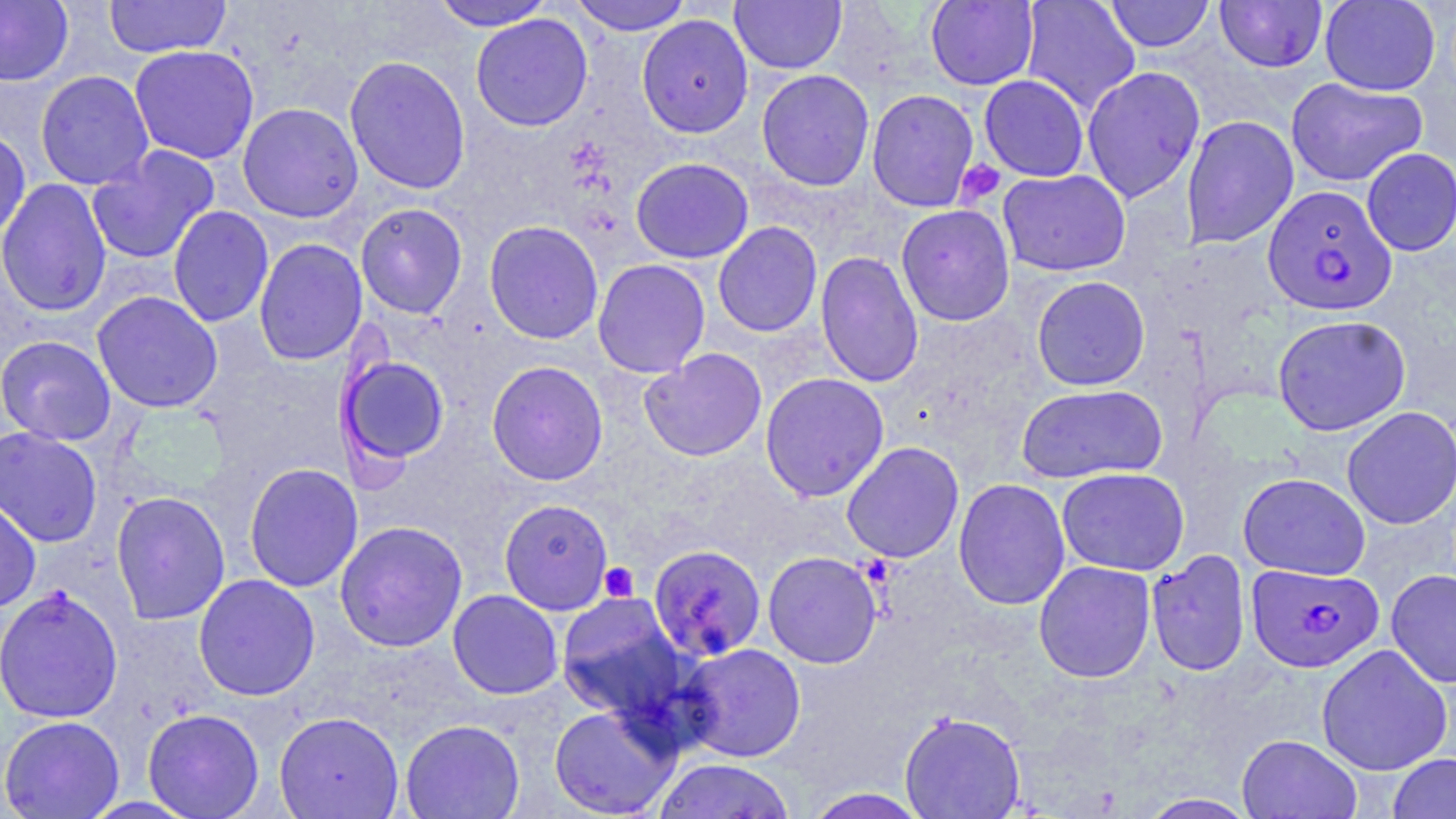

{
  "slide_level_diagnosis": "Plasmodium falciparum",
  "platelet_locations": "approximate bounding boxes as (x1,y1)-(x2,y2) corner pairs in pixels: (956,160)-(1006,205), (599,562)-(639,602)",
  "plasmodium_falciparum_infected_red_blood_cell_locations": "approximate bounding boxes as (x1,y1)-(x2,y2) corner pairs in pixels: (1263,185)-(1397,316), (1246,563)-(1383,672)",
  "uninfected_red_blood_cell_locations": "approximate bounding boxes as (x1,y1)-(x2,y2) corner pairs in pixels: (0,0)-(74,86), (103,0)-(232,59), (568,0)-(694,36), (730,0)-(847,74), (925,0)-(1038,91), (1019,0)-(1141,113), (1104,0)-(1216,52), (1214,0)-(1328,73), (1319,0)-(1441,96), (429,1)-(556,31), (470,14)-(593,131), (636,14)-(753,138), (129,44)-(260,164), (344,55)-(471,195), (1081,66)-(1205,202), (34,69)-(155,190), (756,69)-(875,191), (978,74)-(1089,182), (1286,76)-(1427,187), (866,88)-(980,212), (237,102)-(363,223), (1180,114)-(1300,249), (0,127)-(31,241), (86,145)-(221,265), (1361,147)-(1456,256), (630,157)-(754,263), (998,169)-(1131,276), (0,178)-(112,317), (355,203)-(468,320), (896,204)-(1015,326), (167,205)-(275,328), (484,220)-(604,344), (713,221)-(822,337), (253,237)-(368,366), (815,251)-(924,389), (592,258)-(711,378), (1031,275)-(1151,391), (92,291)-(222,413), (1272,314)-(1411,436), (0,335)-(117,446), (640,347)-(767,462), (336,353)-(450,467), (486,360)-(608,486), (760,372)-(890,502), (1016,383)-(1167,484), (1341,406)-(1456,530), (0,426)-(103,548), (841,441)-(964,563), (243,462)-(363,593), (1057,467)-(1190,576), (1238,472)-(1371,580), (953,478)-(1070,610), (110,490)-(231,626), (0,497)-(41,613), (499,498)-(614,615), (334,520)-(468,652), (648,544)-(766,661), (1145,550)-(1251,677), (763,551)-(882,669), (1033,560)-(1156,683), (1386,568)-(1456,688), (193,573)-(320,701), (0,585)-(124,723), (448,589)-(563,699), (555,592)-(689,724), (676,643)-(807,762), (1316,644)-(1453,776), (548,703)-(679,818), (142,708)-(265,818), (899,710)-(1025,818), (274,711)-(404,818), (1,715)-(125,818), (400,719)-(525,818), (1237,734)-(1361,819), (1387,752)-(1456,819), (651,758)-(796,819), (803,787)-(931,819), (1136,793)-(1261,818)",
  "field_of_view": "single",
  "magnification": "1000x",
  "stain": "May-Grünwald-Giemsa",
  "preparation": "thin blood smear",
  "image_size": "1456×819 pixels",
  "modality": "optical microscopy"
}